Point out each leukocyte.
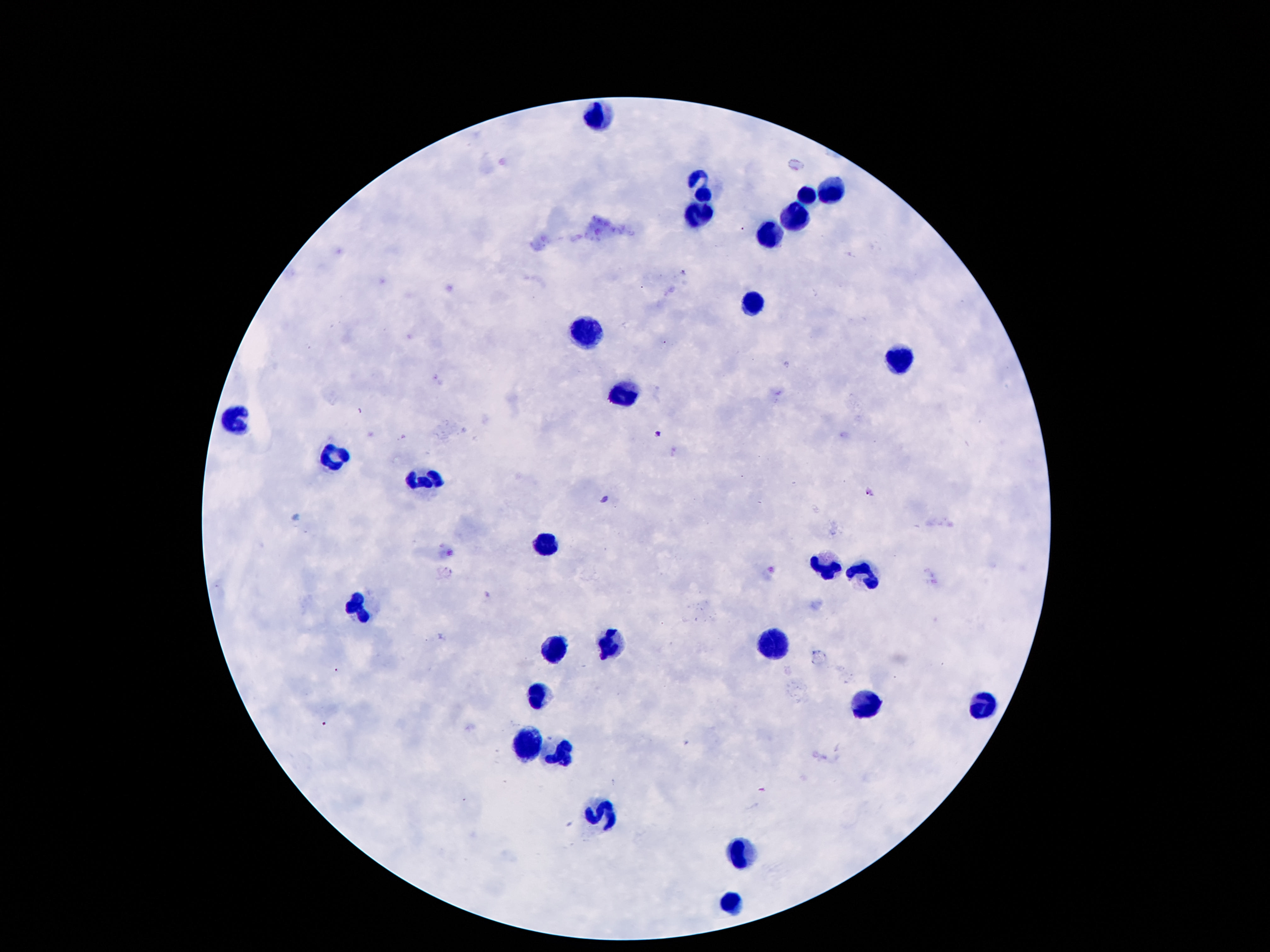

Approximate centers as [x, y] in pixels.
Leukocytes: [598, 119], [702, 189], [832, 191], [808, 196], [699, 214], [797, 215], [770, 236], [755, 302], [582, 331], [898, 363], [620, 397], [237, 419], [332, 461], [425, 483], [547, 545], [825, 565], [863, 578], [354, 608], [781, 644], [609, 646], [556, 649], [536, 697], [980, 706], [865, 708], [525, 746], [562, 755], [604, 810], [744, 856], [732, 907].

Patient malaria status: not infected. 100x magnification. Image is 1270×952 pixels. Smartphone photograph taken through the microscope eyepiece. Giemsa-stained preparation. One field from this slide. Thick peripheral-blood smear.